Assess this cell for malaria.
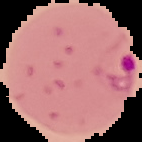

Parasitized.

{
  "image_size": "142×142 pixels",
  "image_type": "cell region segmented out of the field of view; surrounding area masked to black",
  "preparation": "thin blood smear"
}